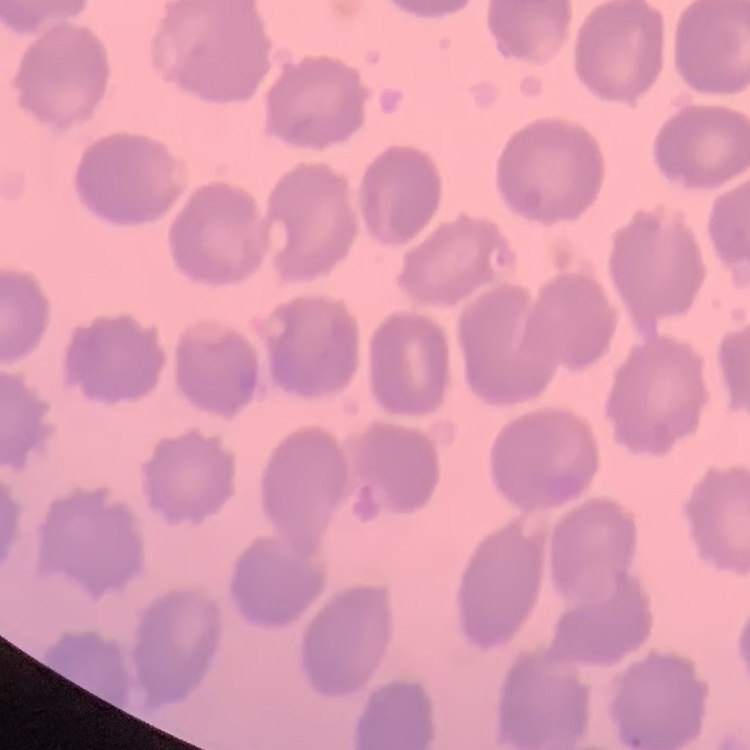
erythrocyte morphology = no rouleaux formation
preparation = thin blood smear
stain = Field's or Giemsa
image type = one tile cut from a larger photomicrograph